Outline each blood parasite and name the species.
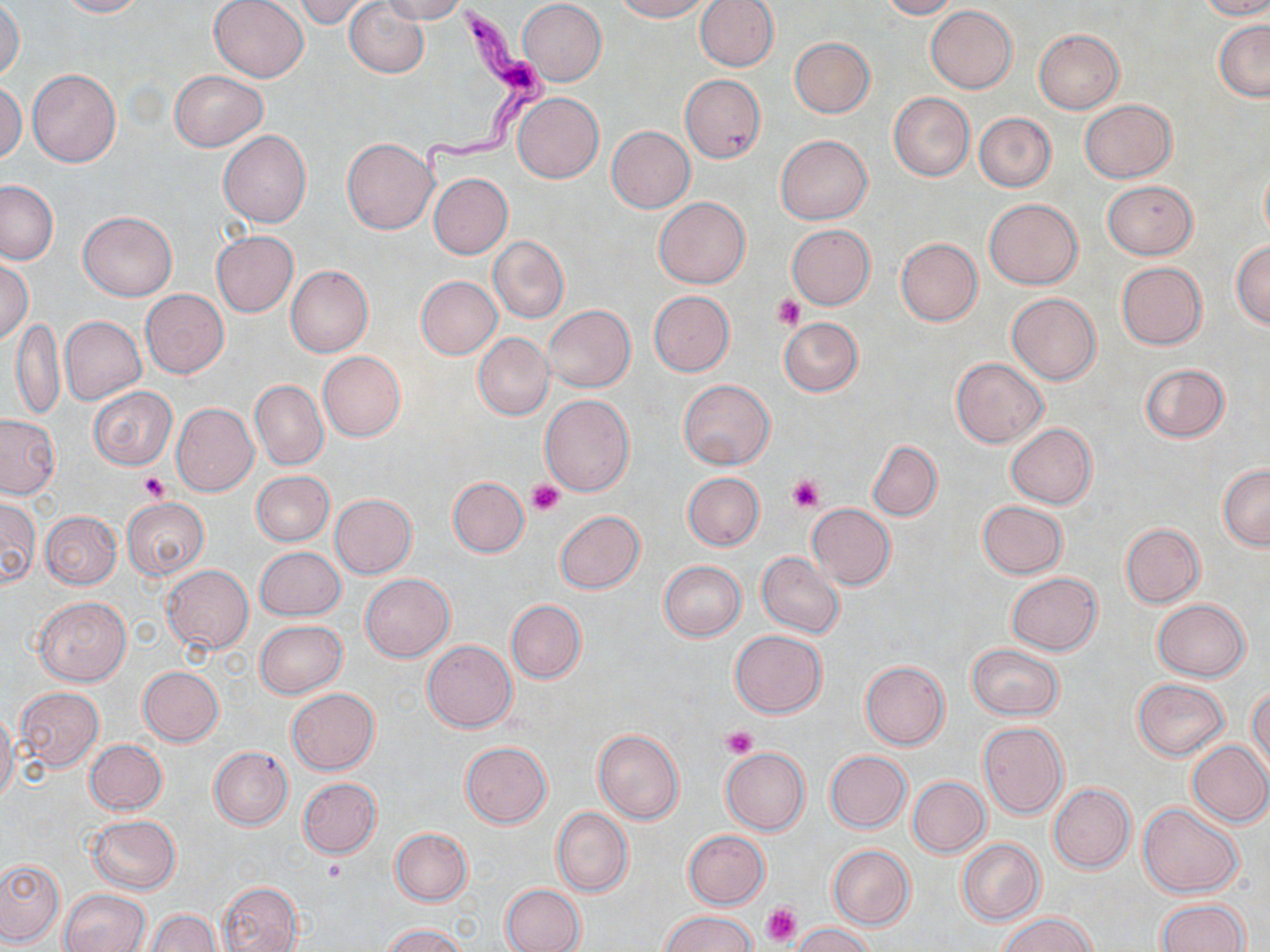
Approximate bounding boxes as [x1, y1, x2, y2] in pixels.
Trypanosoma brucei: [419, 0, 555, 182].
No Plasmodium falciparum, Plasmodium ovale, Plasmodium malariae, Plasmodium vivax, or Babesia divergens observed.

Summary:
  - Platelet locations: [773, 295, 805, 329], [139, 472, 170, 502], [788, 474, 825, 513], [526, 480, 564, 517], [723, 725, 758, 758], [321, 860, 349, 884], [761, 902, 802, 947]
  - Uninfected red blood cell locations: [56, 0, 145, 17], [209, 0, 309, 82], [295, 0, 376, 28], [378, 0, 467, 24], [612, 0, 710, 21], [694, 0, 779, 71], [880, 0, 959, 19], [1199, 0, 1270, 20], [518, 1, 607, 86], [344, 2, 429, 77], [0, 3, 25, 80], [926, 5, 1017, 92], [1214, 20, 1270, 101], [1033, 29, 1124, 114], [790, 37, 875, 118], [27, 68, 121, 167], [170, 70, 267, 151], [678, 74, 766, 164], [0, 82, 26, 163], [889, 91, 974, 181], [514, 93, 603, 183], [1081, 99, 1176, 183], [974, 113, 1057, 192], [606, 125, 696, 213], [218, 131, 311, 227], [775, 134, 872, 224], [342, 138, 438, 234], [1260, 163, 1270, 242], [429, 173, 512, 258], [0, 180, 57, 264], [1102, 180, 1196, 259], [655, 197, 750, 288], [984, 198, 1084, 290], [79, 211, 177, 301], [786, 224, 875, 309], [212, 231, 298, 317], [488, 235, 569, 323], [896, 238, 983, 326], [1231, 241, 1270, 329], [0, 258, 33, 345], [1116, 262, 1207, 349], [286, 266, 373, 357], [416, 276, 502, 358], [141, 290, 228, 378], [649, 291, 734, 376], [1007, 293, 1101, 384], [544, 306, 635, 391], [10, 316, 65, 420], [60, 316, 146, 405], [780, 316, 863, 396], [473, 333, 554, 420], [318, 352, 406, 442], [950, 356, 1048, 448], [1140, 363, 1230, 443], [679, 379, 774, 469], [250, 380, 327, 469], [87, 386, 178, 469], [540, 394, 634, 495], [172, 403, 258, 496], [0, 414, 60, 498], [1006, 423, 1097, 508], [867, 441, 942, 520], [1218, 464, 1270, 550], [251, 470, 333, 545], [683, 472, 764, 550], [448, 477, 528, 558], [329, 494, 417, 578], [0, 498, 40, 589], [122, 498, 210, 579], [977, 500, 1067, 579], [807, 503, 896, 589], [41, 510, 121, 589], [555, 510, 644, 594], [1121, 523, 1205, 608], [255, 546, 345, 621], [756, 552, 845, 638], [659, 561, 746, 640], [162, 565, 254, 654], [1006, 572, 1103, 655], [360, 573, 455, 662], [34, 595, 131, 686], [506, 599, 586, 683], [1153, 599, 1251, 681], [254, 620, 348, 699], [730, 630, 828, 718], [422, 641, 517, 732], [967, 643, 1063, 721], [860, 660, 951, 750], [137, 666, 224, 746], [1132, 678, 1230, 760], [1248, 686, 1269, 779], [287, 687, 380, 774], [14, 688, 104, 771], [0, 709, 19, 806], [977, 721, 1068, 820], [593, 728, 684, 823], [85, 739, 167, 814], [1186, 740, 1270, 827], [460, 741, 551, 828], [209, 746, 293, 829], [720, 747, 810, 834], [825, 751, 911, 832], [908, 777, 990, 858], [297, 778, 381, 858], [1049, 783, 1135, 872], [1139, 802, 1244, 898], [552, 807, 633, 897], [88, 815, 181, 894], [391, 828, 473, 905], [684, 830, 769, 909], [957, 839, 1046, 925], [827, 845, 915, 929], [0, 859, 65, 945], [218, 882, 302, 952], [501, 884, 585, 952], [59, 889, 151, 952], [1155, 899, 1250, 952], [146, 910, 221, 952], [659, 911, 758, 952], [998, 912, 1098, 952], [793, 923, 874, 952], [381, 924, 468, 952]
  - Slide-level diagnosis: Trypanosoma brucei
  - Image size: 1270×952 pixels
  - Magnification: 1000x
  - Stain: May-Grünwald-Giemsa
  - Preparation: thin blood film
  - Field of view: single
  - Modality: light microscopy